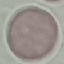
Result: no malaria parasites detected. Photographed with a smartphone camera at the microscope eyepiece. Automatically extracted cell patch, resized to 64 × 64 pixels. Giemsa-stained preparation. Thin blood film.